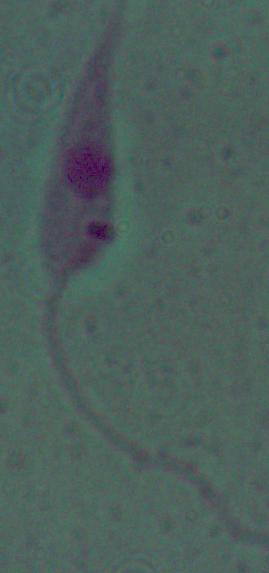

Summary:
  - Magnification: 1000x
  - Identification: Leishmania
  - Modality: micrograph